Locate every Plasmodium parasite.
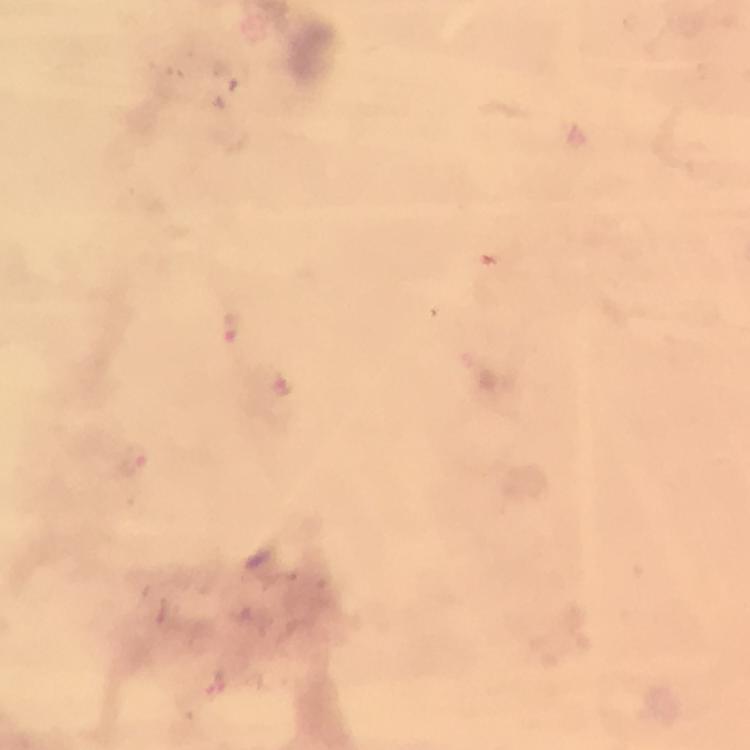
Approximate centers as [x, y] in pixels.
Plasmodium parasites: [230, 325], [283, 387], [135, 462], [215, 679].

Giemsa-stained preparation. Immersion oil applied. Photographed with a smartphone mounted on the microscope. From a diagnostic examination for malaria. At 100x magnification. Thick smear. A crop from one field of view. Image is 750×750 pixels.